Identify the preparation type.
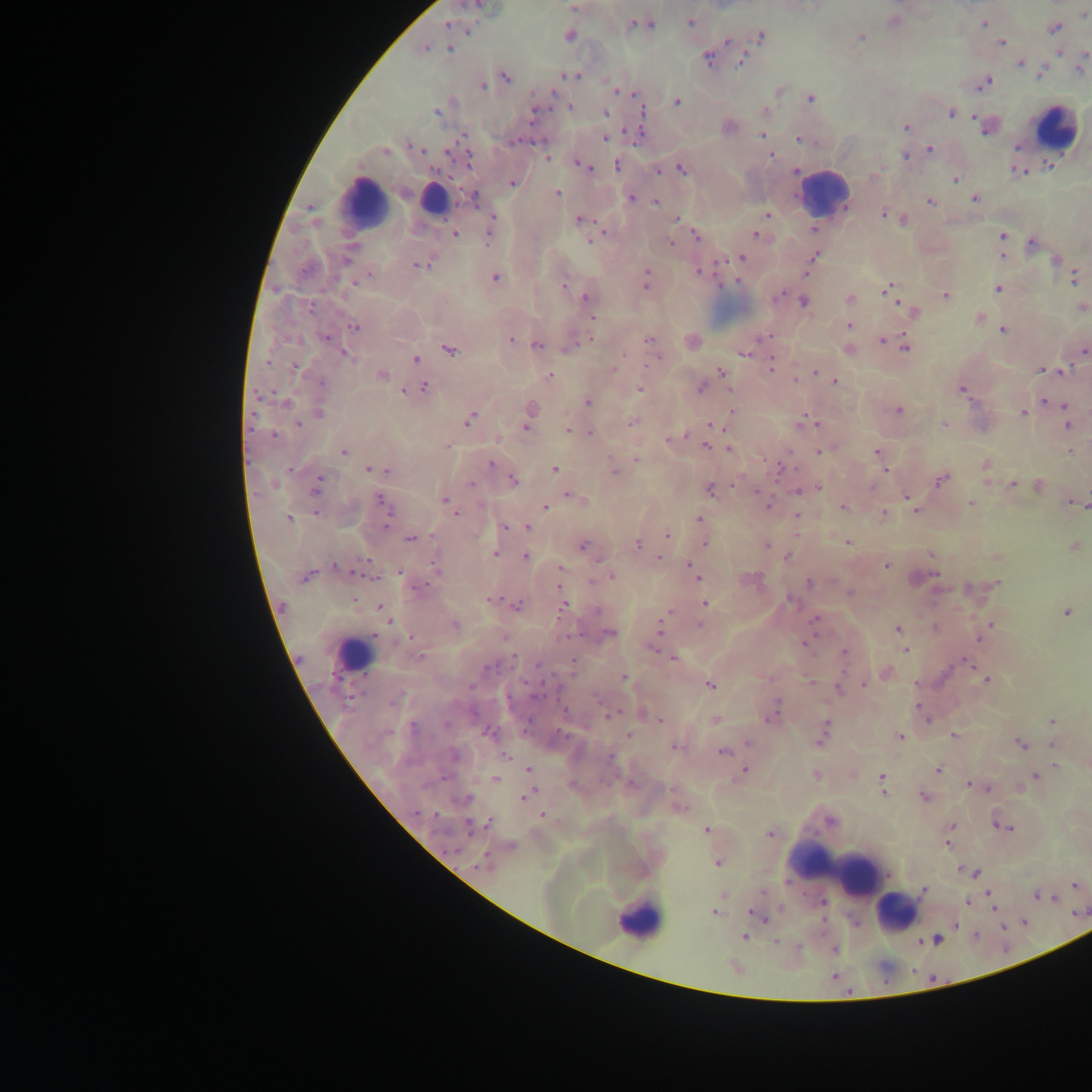

This is a thick smear.

Approximate centers as {x, y} in pixels.
Summary:
  - Leukocyte locations: {1056, 129}, {824, 193}, {433, 200}, {365, 204}, {353, 653}, {831, 862}, {841, 872}, {897, 912}, {638, 920}
  - Plasmodium parasite locations: {474, 5}, {574, 7}, {1083, 14}, {894, 21}, {690, 22}, {984, 23}, {447, 24}, {640, 24}, {1054, 27}, {467, 29}, {568, 35}, {861, 36}, {760, 37}, {727, 41}, {1001, 42}, {449, 47}, {423, 48}, {1058, 51}, {707, 57}, {742, 59}, {1020, 63}, {1080, 68}, {1041, 70}, {570, 75}, {504, 76}, {983, 82}, {481, 86}, {778, 90}, {617, 91}, {635, 94}, {810, 98}, {677, 100}, {570, 106}, {438, 110}, {533, 111}, {950, 111}, {604, 113}, {766, 113}, {988, 125}, {727, 126}, {905, 126}, {636, 133}, {761, 135}, {461, 137}, {605, 138}, {799, 138}, {418, 149}, {930, 150}, {385, 151}, {771, 155}, {906, 155}, {547, 157}, {581, 164}, {617, 165}, {681, 168}, {658, 169}, {1018, 170}, {795, 171}, {955, 179}, {512, 182}, {558, 193}, {974, 197}, {474, 198}, {630, 198}, {930, 200}, {656, 201}, {767, 214}, {883, 214}, {677, 218}, {580, 220}, {902, 220}, {490, 226}, {813, 228}, {455, 234}, {756, 234}, {696, 235}, {1002, 235}, {590, 239}, {670, 242}, {1032, 242}, {1002, 254}, {814, 256}, {740, 257}, {1056, 260}, {418, 263}, {698, 271}, {494, 277}, {1074, 277}, {646, 280}, {737, 280}, {563, 285}, {888, 288}, {998, 288}, {945, 295}, {586, 298}, {849, 299}, {803, 302}, {1081, 307}, {912, 311}, {591, 317}, {978, 318}, {849, 325}, {355, 327}, {1003, 329}, {763, 336}, {325, 337}, {591, 338}, {649, 339}, {510, 340}, {882, 340}, {571, 341}, {692, 341}, {536, 344}, {905, 346}, {448, 349}, {847, 349}, {1083, 350}, {343, 353}, {744, 353}, {415, 358}, {655, 358}, {771, 366}, {294, 367}, {1041, 369}, {612, 370}, {1063, 371}, {722, 372}, {815, 372}, {380, 375}, {549, 375}, {795, 379}, {834, 381}, {701, 386}, {423, 387}, {640, 389}, {962, 389}, {404, 390}, {587, 401}, {1046, 401}, {285, 402}, {1055, 402}, {1064, 406}, {897, 410}, {319, 411}, {732, 411}, {1024, 412}, {528, 415}, {470, 418}, {805, 420}, {631, 423}, {298, 424}, {944, 424}, {710, 425}, {1066, 425}, {568, 429}, {590, 434}, {273, 436}, {672, 439}, {446, 446}, {705, 446}, {728, 448}, {1070, 450}, {821, 451}, {343, 452}, {877, 452}, {637, 458}, {490, 464}, {985, 464}, {554, 468}, {779, 468}, {370, 469}, {381, 469}, {613, 469}, {885, 469}, {941, 478}, {511, 479}, {317, 484}, {1012, 484}, {1038, 485}, {818, 486}, {709, 489}, {798, 489}, {568, 495}, {907, 496}, {381, 501}, {445, 502}, {971, 502}, {1073, 502}, {767, 505}, {843, 506}, {545, 507}, {383, 508}, {915, 509}, {452, 511}, {884, 514}, {797, 515}, {289, 518}, {699, 520}, {505, 526}, {528, 526}, {667, 536}, {410, 538}, {705, 542}, {847, 542}, {637, 544}, {765, 545}, {1073, 546}, {582, 547}, {494, 553}, {931, 554}, {525, 557}, {787, 557}, {996, 557}, {658, 558}, {437, 564}, {887, 565}, {337, 567}, {560, 568}, {691, 569}, {400, 573}, {305, 575}, {611, 576}, {697, 576}, {809, 583}, {996, 583}, {490, 598}, {705, 603}, {516, 605}, {563, 606}, {380, 608}, {1067, 612}, {814, 619}, {699, 624}, {991, 624}, {454, 625}, {659, 628}, {898, 629}, {986, 630}, {609, 633}, {979, 637}, {411, 638}, {804, 643}, {905, 649}, {843, 653}, {673, 658}, {969, 664}, {886, 672}, {624, 678}, {986, 680}, {865, 684}, {709, 685}, {838, 687}, {918, 707}, {643, 712}, {772, 713}, {609, 715}, {651, 717}, {659, 720}, {714, 720}, {1053, 721}, {822, 732}, {488, 733}, {628, 736}, {900, 736}, {953, 736}, {748, 742}, {1020, 744}, {1052, 744}, {675, 746}, {723, 751}, {1055, 766}, {938, 769}, {528, 770}, {744, 770}, {815, 776}, {1035, 776}, {881, 778}, {494, 780}, {969, 784}, {986, 787}, {1018, 787}, {883, 790}, {526, 794}, {923, 796}, {678, 807}, {542, 815}, {487, 824}, {950, 826}, {1008, 828}, {706, 830}, {769, 834}, {948, 834}, {947, 843}, {510, 847}, {717, 862}, {486, 863}, {960, 869}, {966, 870}, {976, 873}, {1075, 884}, {924, 890}, {988, 894}, {1037, 895}, {967, 903}, {714, 912}, {757, 915}, {743, 937}, {936, 940}, {735, 967}
  - Country: Ghana
  - Image size: 1092×1092 pixels
  - Field of view: single
  - Capture: mobile-phone photograph through a microscope